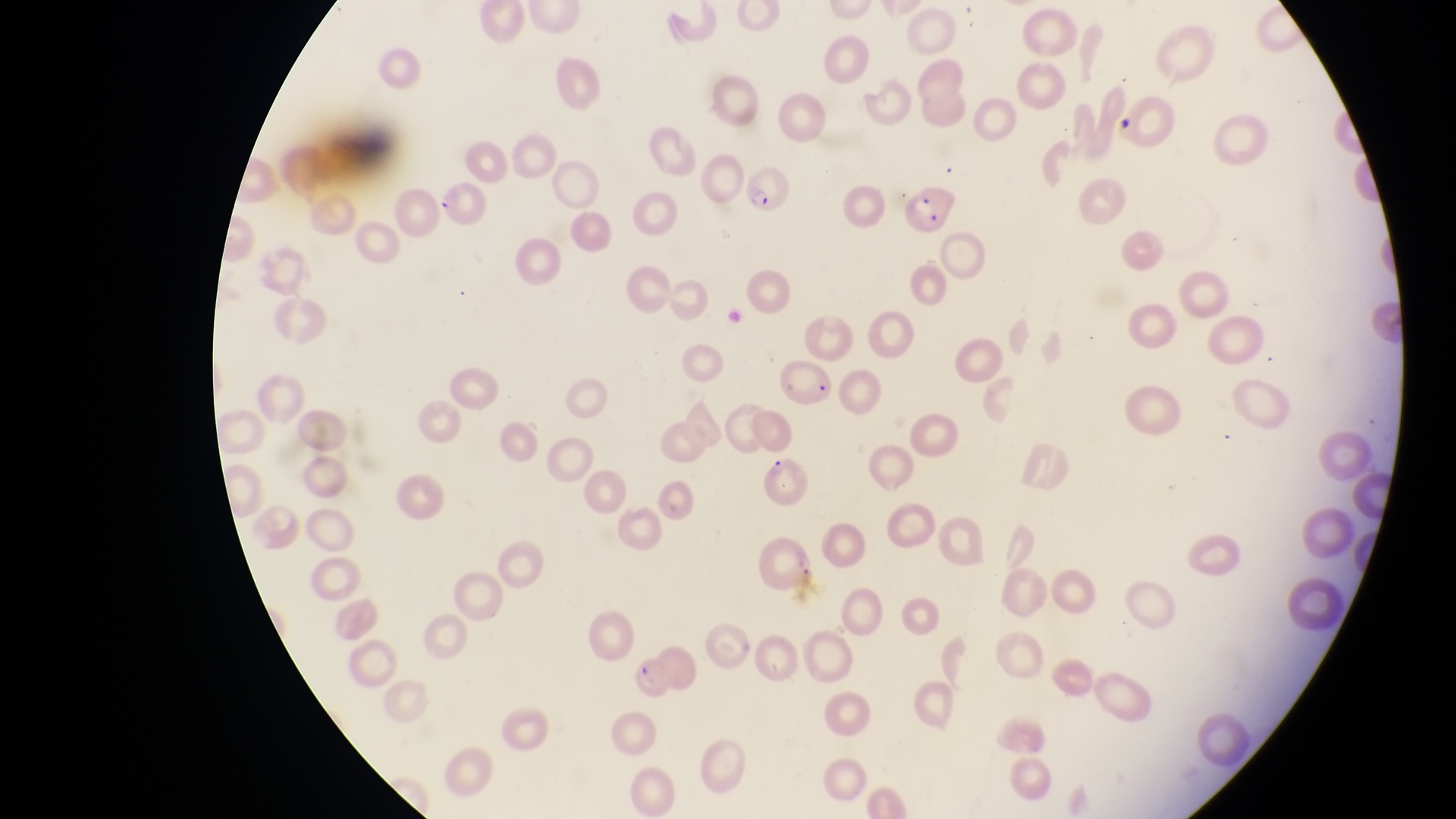 Approximate bounding boxes as (left, top, right, bottom) in pixels. Parasitised red blood cell locations: (740, 166, 795, 218), (433, 177, 491, 226), (898, 178, 958, 238), (629, 657, 688, 706). Image is 1456×819 pixels. Magnification of 1000x. One field of view. Photographed through the eyepiece of an Olympus CX-23 microscope with a smartphone camera. Thin blood smear. Collected in Uganda.